Locate every Plasmodium falciparum parasite and identify its life-cycle stage.
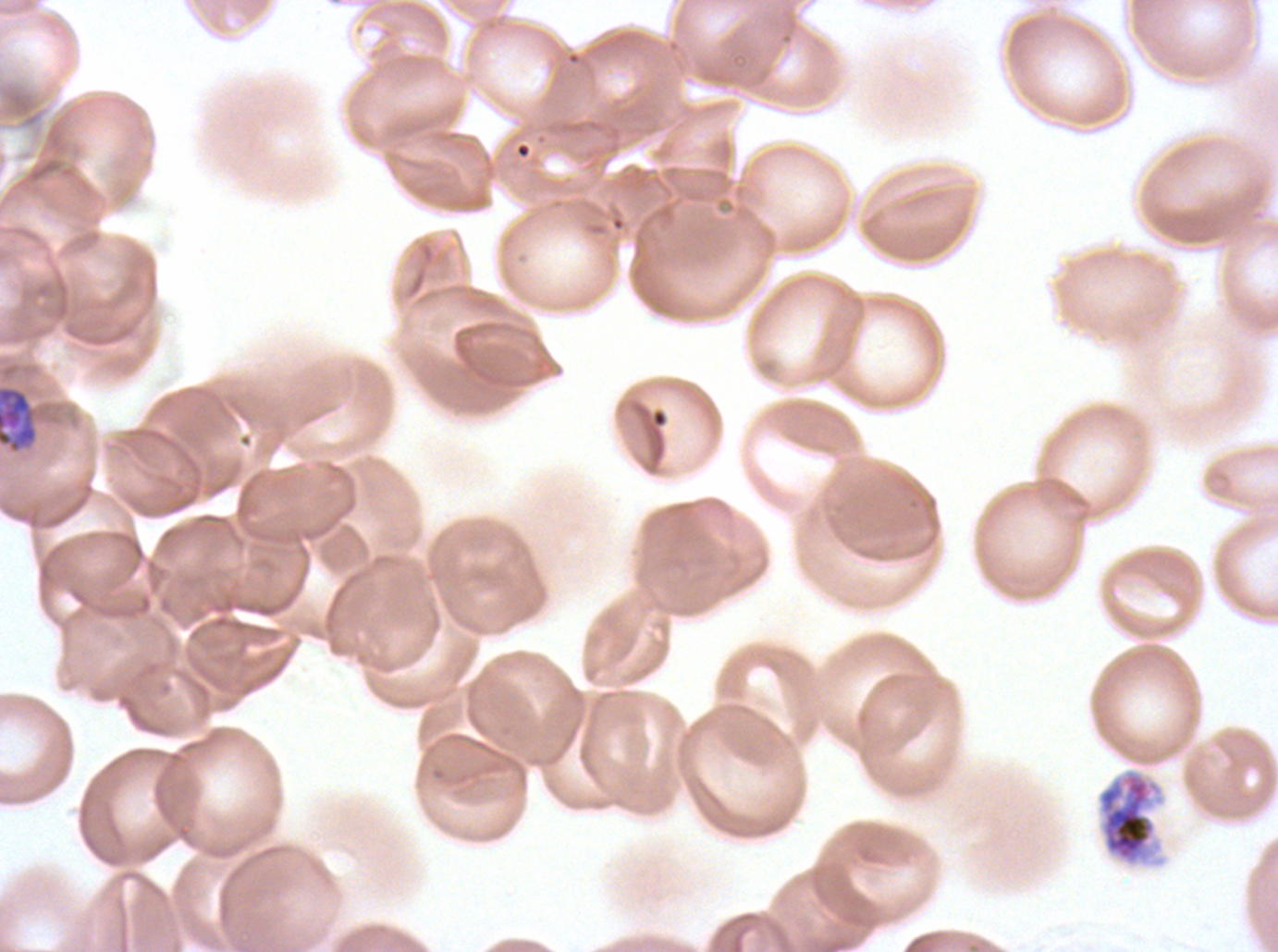
Approximate bounding boxes as [x1, y1, x2, y2] in pixels.
Mid trophozoites: [0, 386, 38, 453].
Late schizonts: [1097, 768, 1163, 867].
No rings, late-ring/early-trophozoite forms, late trophozoites, early schizonts, segmenters, or gametocytes observed.

{
  "image_size": "1278×952 pixels",
  "stain": "Giemsa",
  "life_cycle_stages_observed": "mid trophozoite, late schizont",
  "preparation": "thin blood film",
  "field_of_view": "one sub-image of a larger composite",
  "specimen": "Plasmodium falciparum cultured ex vivo for 24 to 48 hours, from a patient in The Gambia"
}